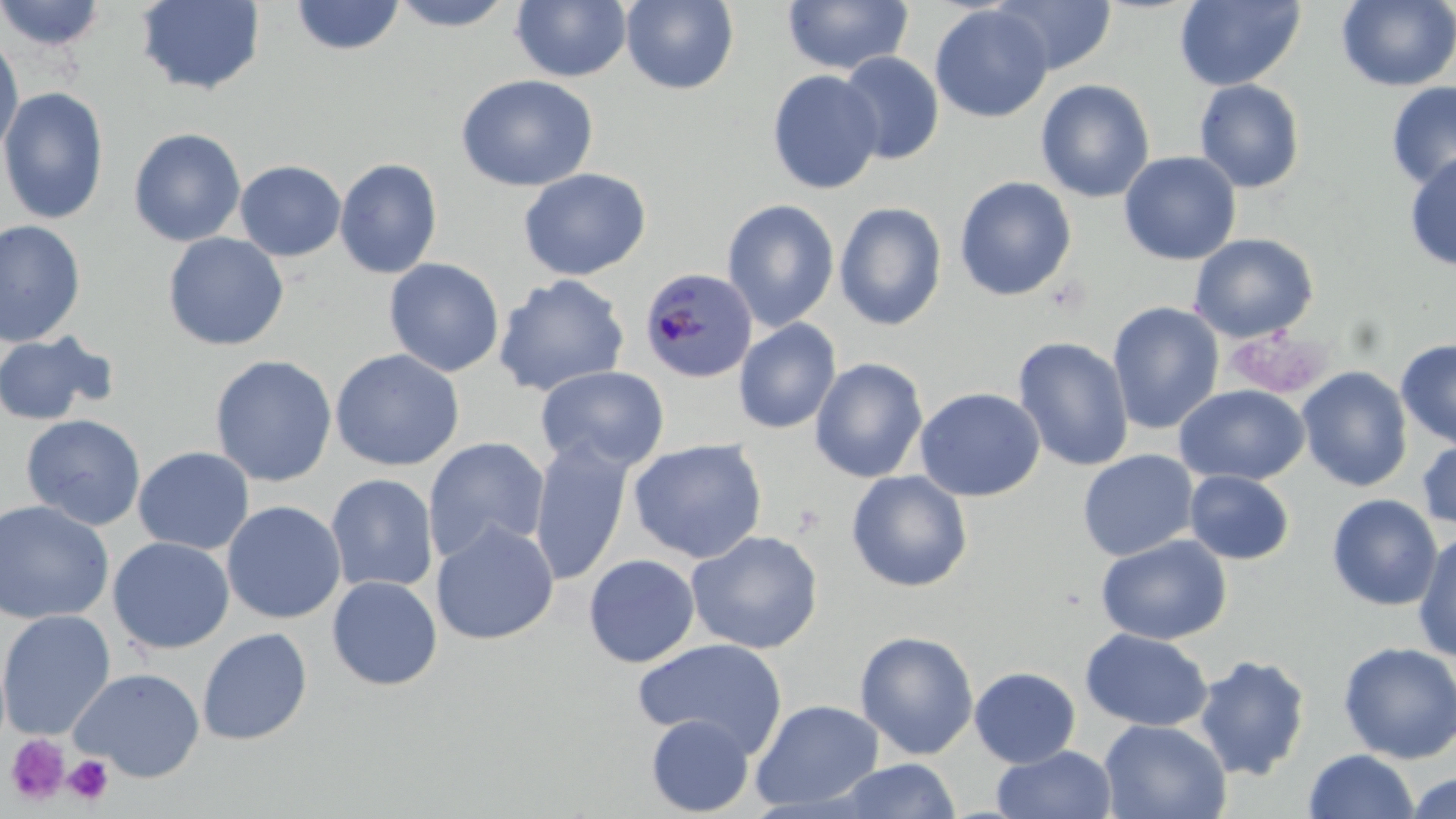 Approximate bounding boxes as (x1,y1)-(x2,y2) corner pairs in pixels. Uninfected red blood cell locations: (0,0)-(109,52), (386,0)-(519,31), (782,0)-(913,76), (991,0)-(1117,75), (1175,0)-(1305,91), (135,1)-(265,96), (290,1)-(406,56), (511,1)-(632,83), (620,1)-(739,95), (1336,1)-(1456,91), (929,4)-(1053,123), (0,30)-(25,160), (837,51)-(944,165), (767,69)-(884,195), (456,74)-(598,192), (1035,79)-(1155,203), (1193,79)-(1306,194), (1386,80)-(1456,194), (0,86)-(109,225), (128,127)-(246,247), (1404,150)-(1456,272), (1119,151)-(1241,265), (333,158)-(442,279), (234,160)-(346,262), (518,168)-(651,281), (953,176)-(1076,301), (721,198)-(840,331), (834,201)-(947,331), (0,220)-(86,347), (162,232)-(289,351), (1189,233)-(1318,343), (383,258)-(504,377), (493,274)-(630,397), (1107,301)-(1225,435), (733,318)-(841,434), (0,330)-(118,426), (1013,336)-(1134,472), (1396,338)-(1456,450), (329,348)-(465,471), (209,354)-(337,488), (810,357)-(928,483), (535,365)-(669,473), (1296,366)-(1413,492), (1174,383)-(1309,486), (915,386)-(1046,502), (21,414)-(147,531), (423,437)-(550,562), (1416,437)-(1456,532), (529,438)-(634,586), (628,438)-(767,564), (133,446)-(254,555), (1077,449)-(1200,561), (846,470)-(973,592), (1184,470)-(1295,565), (325,473)-(439,593), (1326,493)-(1443,611), (0,499)-(114,625), (222,500)-(346,624), (430,521)-(559,645), (686,530)-(823,655), (1413,530)-(1456,663), (1096,534)-(1232,645), (107,537)-(235,655), (583,554)-(700,668), (326,575)-(443,690), (0,610)-(116,740), (197,627)-(312,745), (1079,628)-(1213,731), (854,630)-(979,760), (633,637)-(789,756), (1337,641)-(1456,763), (1194,654)-(1311,781), (969,666)-(1081,768), (71,667)-(206,783), (750,699)-(884,812), (646,715)-(754,816), (1098,719)-(1232,819), (992,744)-(1117,818), (1303,749)-(1420,819), (833,759)-(963,818), (1404,772)-(1455,819). Plasmodium malariae-infected red blood cell locations: (639,268)-(758,384). Platelet locations: (5,734)-(70,805), (64,755)-(113,804). Slide-level diagnosis: Plasmodium malariae. Thin blood film. Image is 1456×819 pixels. Captured at 1000x magnification. May-Grünwald-Giemsa stain. One field of a larger specimen. Optical microscopy.